Comment on the morphology of the erythrocytes.
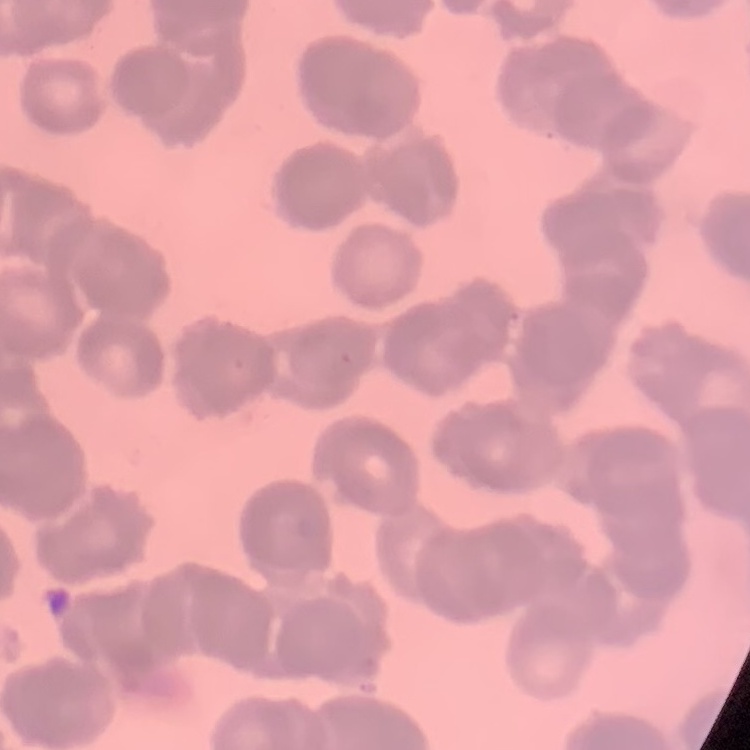

They show rouleaux formation.

Summary:
  - Stain: Field's or Giemsa
  - Preparation: thin peripheral smear
  - Image type: one tile cut from a larger photomicrograph